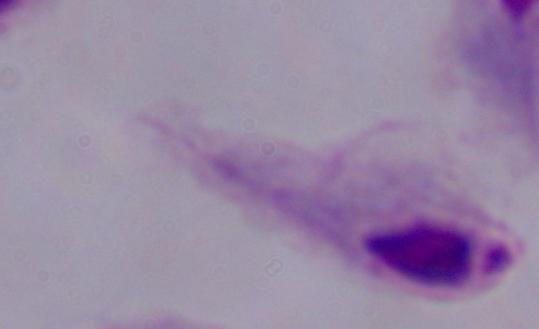 Micrograph. Captured at 1000x magnification. A trichomonad is seen.